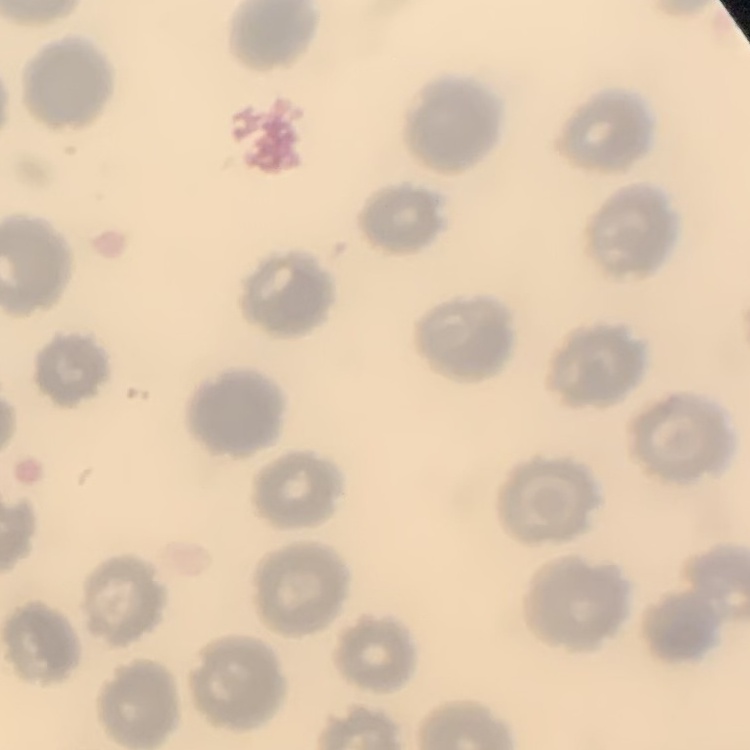
Summary:
  - Erythrocyte morphology: no rouleaux formation
  - Preparation: thin blood film
  - Stain: Field's or Giemsa
  - Image type: one tile cut from a larger photomicrograph